Locate and identify every blood parasite.
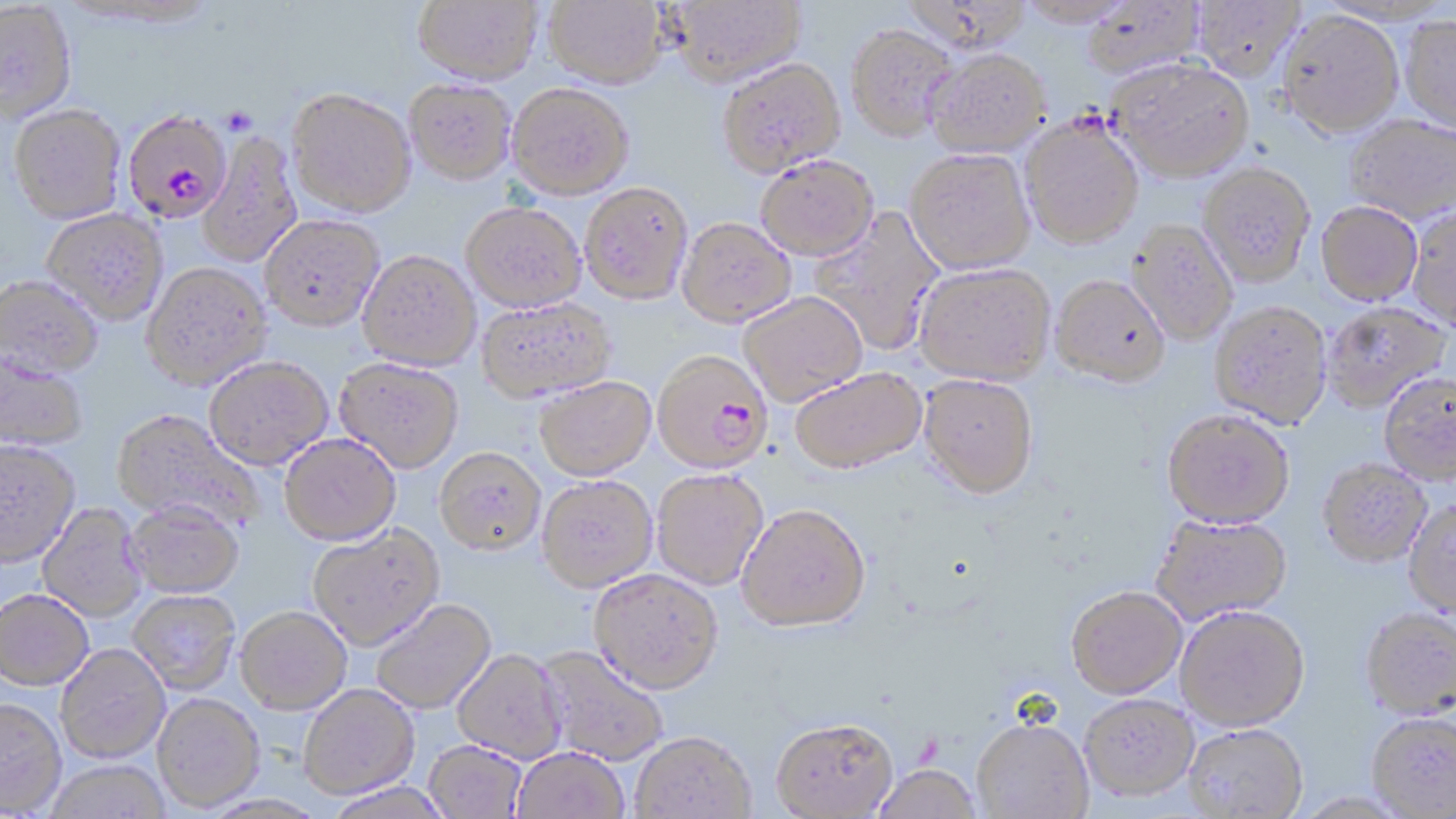

Approximate bounding boxes as (x1,y1)-(x2,y2) corner pairs in pixels.
Plasmodium falciparum-infected red blood cells: (124,112)-(231,223), (651,349)-(772,474).
No Plasmodium ovale, Plasmodium malariae, Plasmodium vivax, Babesia divergens, or Trypanosoma brucei observed.

Uninfected red blood cell locations: (411,0)-(543,86), (544,0)-(666,88), (664,0)-(805,87), (1016,0)-(1135,27), (1081,0)-(1206,81), (1191,1)-(1305,80), (0,4)-(78,126), (1277,10)-(1404,137), (1401,16)-(1456,134), (846,24)-(960,141), (924,48)-(1050,157), (717,57)-(846,177), (1109,58)-(1254,182), (404,79)-(516,184), (507,82)-(634,199), (287,90)-(416,219), (8,107)-(126,227), (1344,114)-(1456,223), (1019,116)-(1144,248), (198,131)-(303,269), (905,149)-(1036,273), (755,154)-(878,259), (1199,162)-(1315,286), (579,182)-(693,305), (1316,201)-(1422,305), (461,202)-(586,313), (1407,204)-(1456,332), (809,209)-(945,356), (42,210)-(169,327), (260,216)-(384,334), (677,216)-(796,326), (1127,220)-(1238,346), (357,251)-(482,372), (915,263)-(1055,384), (142,265)-(273,393), (1051,274)-(1170,386), (0,278)-(103,383), (737,292)-(868,407), (476,298)-(616,404), (1209,299)-(1332,428), (1322,301)-(1450,412), (0,357)-(87,453), (333,359)-(463,475), (204,360)-(333,473), (790,366)-(927,473), (1379,372)-(1456,484), (919,373)-(1039,497), (534,376)-(656,481), (1162,408)-(1294,527), (111,411)-(264,532), (278,436)-(401,548), (0,442)-(81,571), (434,448)-(545,558), (1318,458)-(1432,567), (651,469)-(768,590), (537,476)-(658,593), (1403,497)-(1456,616), (737,503)-(871,631), (37,504)-(148,623), (124,505)-(245,601), (1150,513)-(1292,625), (307,526)-(445,653), (588,568)-(723,694), (1066,586)-(1187,698), (0,591)-(93,692), (128,592)-(240,695), (370,599)-(497,715), (1175,604)-(1310,731), (1360,607)-(1456,719), (236,608)-(352,716), (55,645)-(171,764), (535,645)-(669,766), (452,649)-(568,764), (299,684)-(420,799), (152,694)-(265,813), (1080,694)-(1199,801), (0,699)-(66,816), (1366,712)-(1456,817), (770,716)-(899,817), (972,716)-(1094,818), (1184,723)-(1308,819), (630,731)-(756,819), (424,740)-(526,818), (512,748)-(629,819), (44,760)-(171,819), (870,763)-(982,819), (324,781)-(454,819). Platelet locations: (221,107)-(256,137). Slide-level diagnosis: Plasmodium falciparum. May-Grünwald-Giemsa-stained preparation. Single field of view. Image is 1456×819 pixels. Optical microscopy. 1000x magnification. Thin blood smear.